Report the malaria status of this cell.
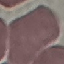

Uninfected.

{
  "preparation": "thin blood smear",
  "stain": "Giemsa",
  "image_type": "automatically extracted cell patch, resized to 64 × 64 pixels",
  "capture": "smartphone through the microscope eyepiece"
}